Identify the parasite.
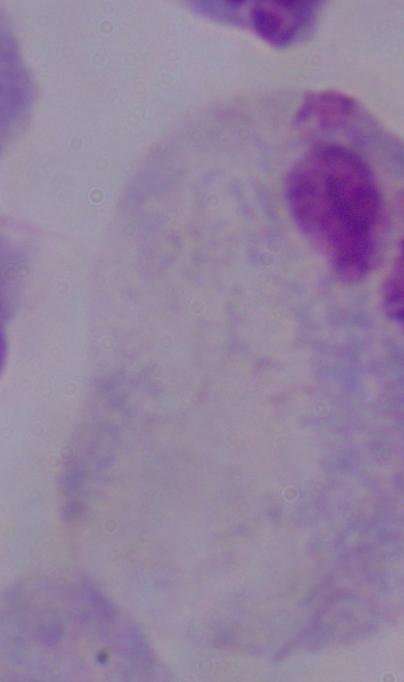
This is a trichomonad.

1000x magnification. Micrograph.